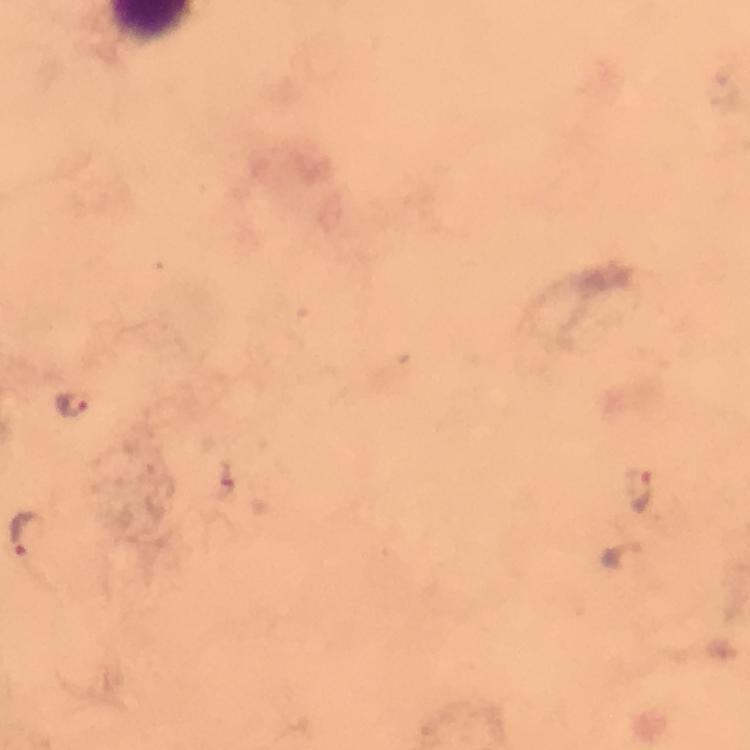
malaria parasite locations = approximate centers as [x, y] in pixels: [72, 404], [641, 490], [28, 534]
image size = 750×750 pixels
preparation = thick smear
magnification = 100x
stain = Giemsa
capture = smartphone mounted on the microscope
cropped from = a single field of view
context = from a diagnostic examination for malaria
immersion oil = applied